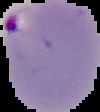
malaria status = parasitized
image type = segmented cell region on a black background
image size = 100×112 pixels
preparation = thin blood smear